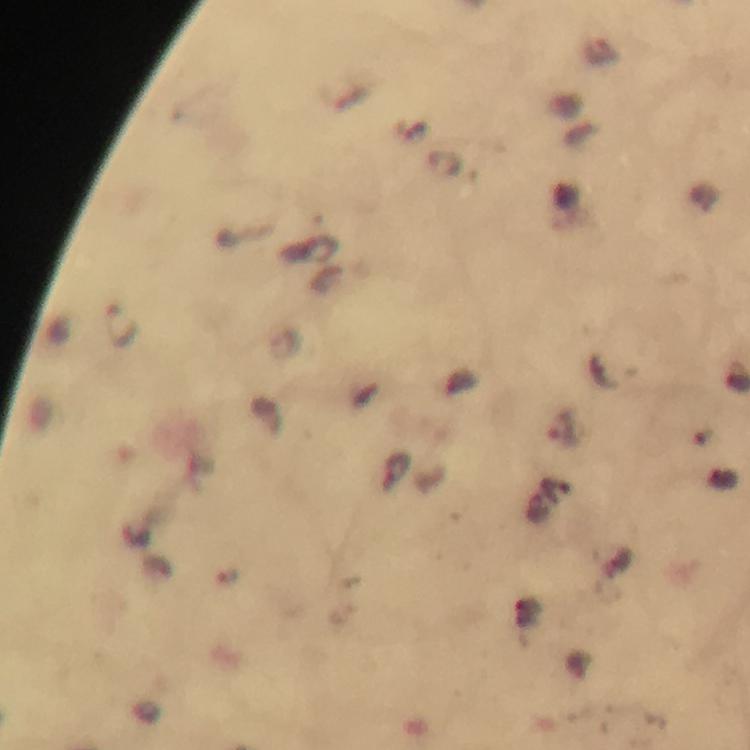

cropped from = one field of view
immersion oil = applied
magnification = 100x
malaria parasite locations = approximate centers as (x, y) in pixels: (119, 326)
image size = 750×750 pixels
stain = Giemsa
preparation = thick blood film
capture = smartphone mounted on the microscope
context = from a diagnostic examination for malaria